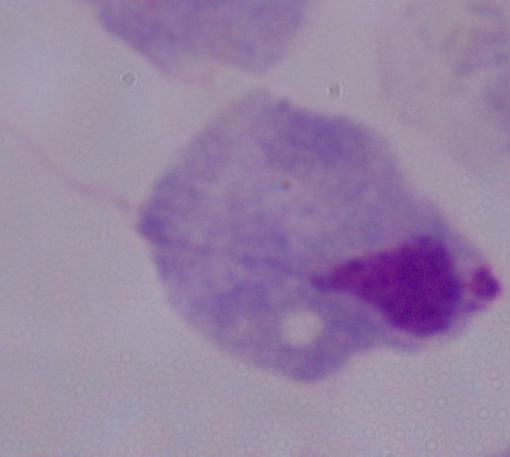

{
  "modality": "photomicrograph",
  "identification": "trichomonad",
  "magnification": "1000x"
}